Identify the preparation type.
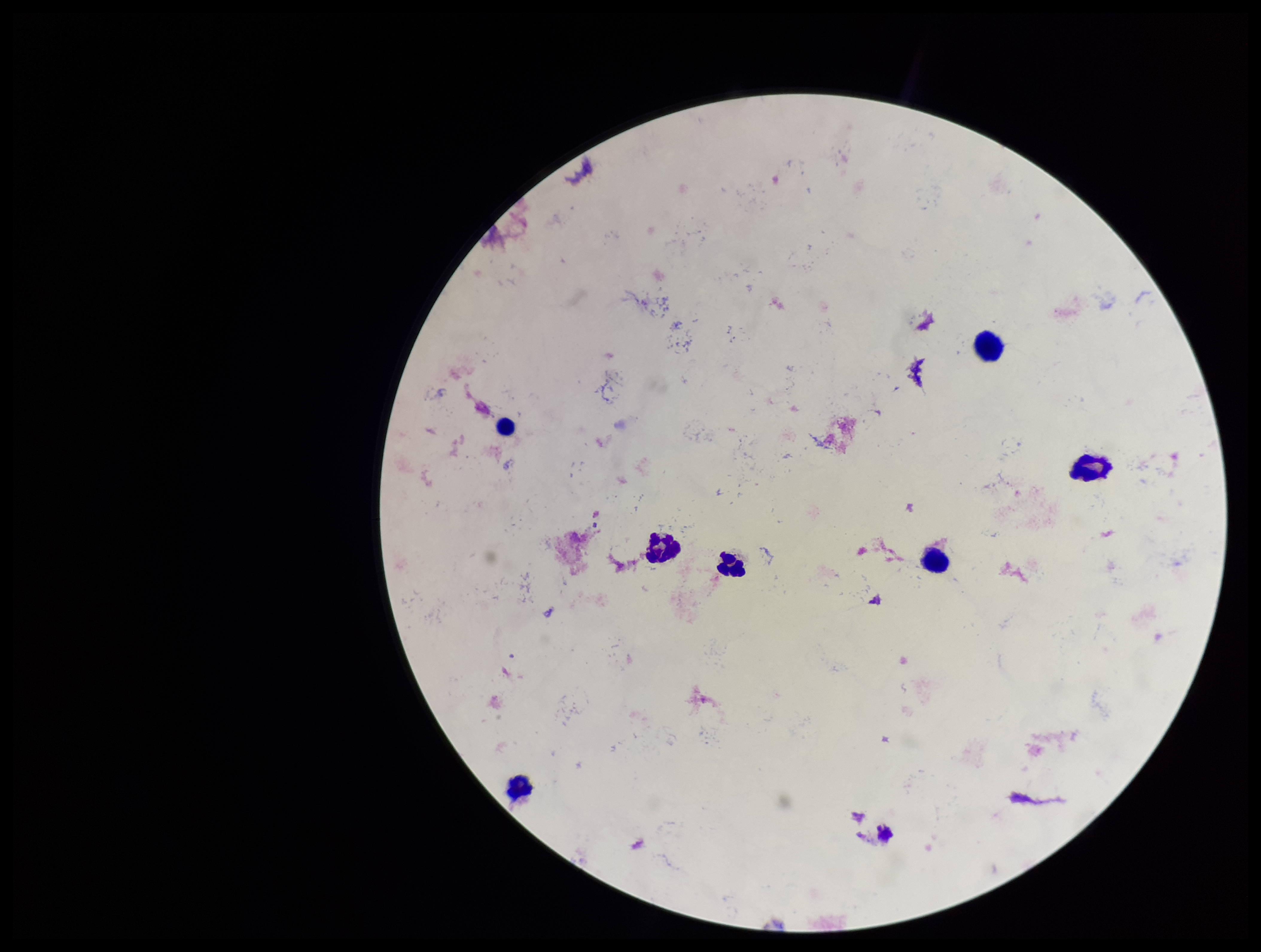
Thick.

Summary:
  - Image size: 1261×952 pixels
  - Patient malaria status: negative
  - Capture: smartphone photograph through the microscope eyepiece
  - Leukocyte count: 7
  - Plasmodium parasites: none detected
  - Stain: Giemsa
  - Field of view: one from this slide
  - Parasite count: 0